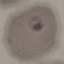
Malaria status: parasitized. Giemsa stain. Automatically extracted cell patch, resized to 64 × 64 pixels. Thin blood smear. Acquired by smartphone through the microscope eyepiece.